Report the malaria status of this cell.
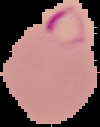
Parasitized.

Image is 100×127 pixels. From a thin blood smear. The area outside the segmented cell region is set to black.